State which parasite is depicted.
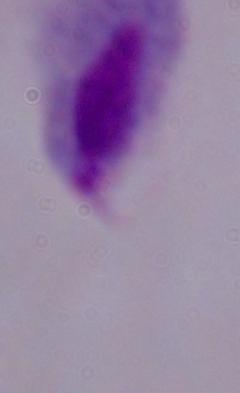
This is a trichomonad.

Captured at 1000x magnification. Micrograph.